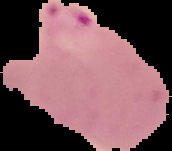

preparation = thin blood film
result = Plasmodium parasites detected
image type = segmented cell region on a black background
image size = 172×151 pixels